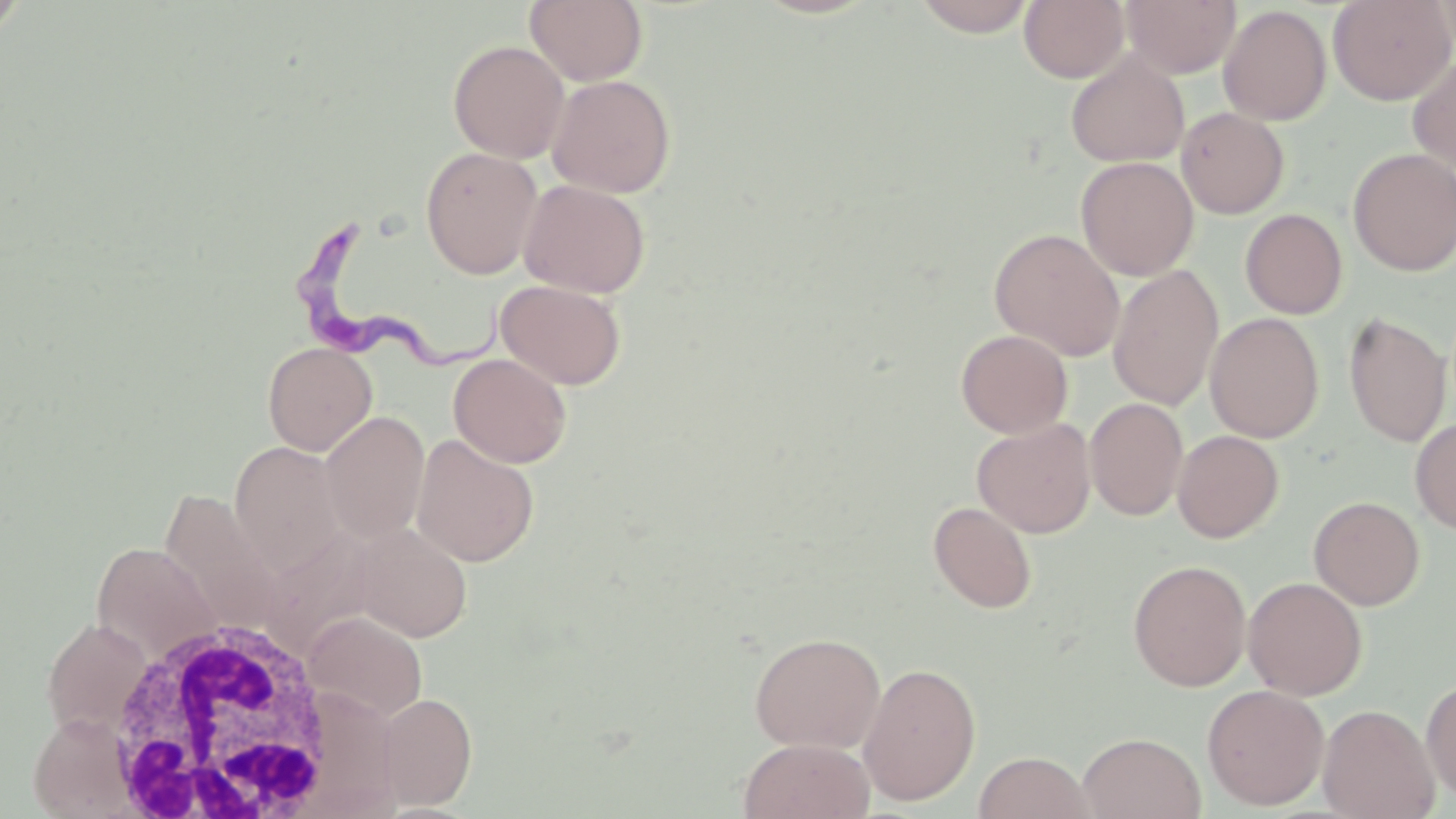

Summary:
  - Coordinate format: approximate bounding boxes as (x1,y1)-(x2,y2) corner pairs in pixels
  - Uninfected red blood cell locations: (913,0)-(1038,36), (1019,0)-(1129,83), (1122,0)-(1241,78), (1328,0)-(1456,105), (0,1)-(26,47), (525,1)-(648,85), (1219,5)-(1332,125), (448,40)-(570,162), (1065,50)-(1189,168), (1408,56)-(1456,175), (546,74)-(676,198), (1176,107)-(1290,219), (420,146)-(543,278), (1348,148)-(1456,276), (1076,156)-(1198,280), (518,179)-(651,298), (1240,208)-(1347,319), (989,228)-(1125,360), (1108,264)-(1224,411), (495,279)-(627,389), (1343,311)-(1452,448), (1205,312)-(1325,442), (955,329)-(1073,438), (262,342)-(378,456), (448,353)-(572,468), (1085,397)-(1188,521), (320,411)-(430,544), (1410,416)-(1456,535), (972,418)-(1095,537), (1173,430)-(1284,542), (412,433)-(539,567), (229,441)-(347,576), (159,490)-(282,630), (1308,495)-(1425,610), (928,501)-(1037,614), (352,524)-(473,642), (260,529)-(378,655), (91,543)-(222,664), (1128,558)-(1251,691), (1243,576)-(1367,700), (303,611)-(428,723), (41,619)-(152,738), (749,631)-(886,753), (858,662)-(981,805), (1421,676)-(1456,803), (1202,683)-(1330,810), (377,693)-(478,809), (1317,704)-(1440,818), (29,712)-(137,818), (1077,732)-(1206,819), (738,738)-(875,819), (973,751)-(1095,819)
  - Trypanosoma brucei locations: (294,215)-(516,379)
  - White blood cell locations: (105,615)-(342,816)
  - Slide-level diagnosis: Trypanosoma brucei
  - Preparation: thin blood smear
  - Modality: optical microscopy
  - Image size: 1456×819 pixels
  - Magnification: 1000x
  - Stain: May-Grünwald-Giemsa
  - Field of view: single